Locate and identify every blood parasite.
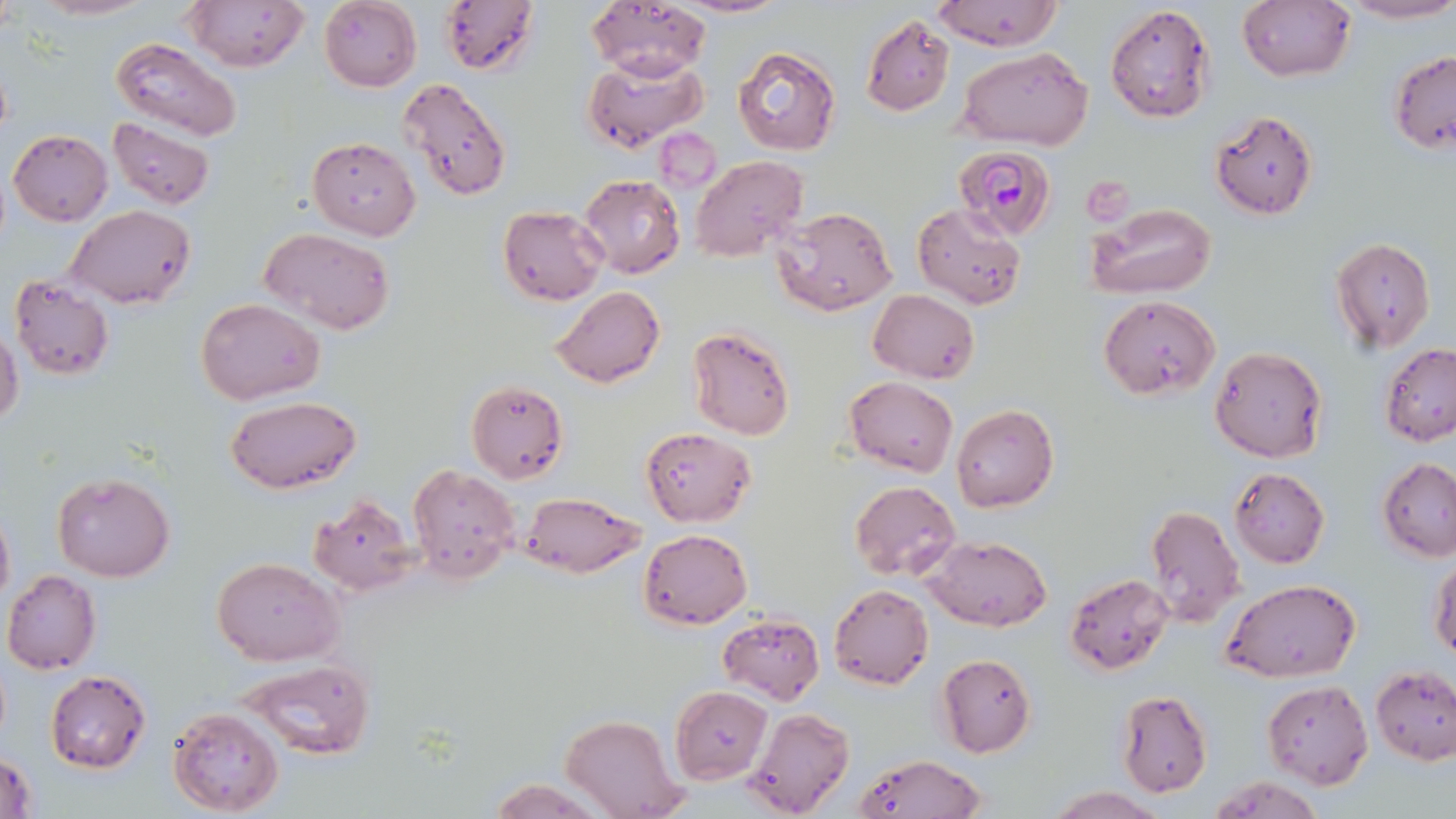

Approximate bounding boxes as (x1,y1)-(x2,y2) corner pairs in pixels.
Plasmodium falciparum-infected red blood cells: (954,145)-(1059,240).
No Plasmodium ovale, Plasmodium malariae, Plasmodium vivax, Babesia divergens, or Trypanosoma brucei observed.

Uninfected red blood cell locations: (27,0)-(157,21), (319,0)-(422,91), (439,0)-(539,76), (675,0)-(788,18), (931,0)-(1063,51), (1335,0)-(1456,24), (183,1)-(309,71), (585,1)-(711,81), (1237,2)-(1355,82), (1105,4)-(1213,123), (862,16)-(953,115), (110,37)-(244,143), (730,45)-(842,158), (958,46)-(1094,148), (1388,50)-(1456,154), (580,56)-(708,153), (397,76)-(513,202), (1211,110)-(1318,220), (108,120)-(215,210), (655,127)-(720,193), (8,129)-(111,226), (307,137)-(420,240), (691,156)-(807,262), (579,175)-(685,277), (911,203)-(1028,311), (1087,203)-(1216,299), (68,205)-(196,309), (498,206)-(607,304), (771,206)-(897,316), (257,227)-(396,335), (1331,238)-(1436,354), (9,275)-(115,381), (552,285)-(665,388), (869,290)-(979,383), (1097,295)-(1220,399), (196,297)-(325,404), (0,326)-(23,430), (686,326)-(795,440), (1381,344)-(1456,446), (1209,345)-(1328,464), (845,375)-(957,477), (465,379)-(568,483), (225,396)-(361,495), (951,405)-(1059,514), (642,427)-(756,526), (1378,457)-(1456,562), (407,465)-(520,582), (1229,467)-(1330,567), (52,471)-(176,584), (848,481)-(961,579), (521,491)-(645,579), (307,495)-(417,596), (0,499)-(13,612), (1144,504)-(1245,627), (639,528)-(752,629), (920,535)-(1052,632), (212,556)-(343,666), (1429,556)-(1456,659), (2,570)-(100,675), (1064,572)-(1175,674), (1222,577)-(1362,682), (828,582)-(933,690), (718,612)-(825,705), (936,654)-(1036,757), (240,660)-(373,764), (1371,666)-(1456,764), (44,669)-(151,773), (1262,679)-(1374,789), (669,688)-(771,783), (1115,689)-(1213,798), (167,705)-(285,816), (744,707)-(854,819), (560,715)-(686,819), (852,753)-(989,818), (0,754)-(37,819), (1204,775)-(1324,818), (485,776)-(607,817), (1042,787)-(1169,819). Slide-level diagnosis: Plasmodium falciparum. Optical microscopy. Single field of view. Thin blood smear. May-Grünwald-Giemsa stain. 1000x magnification. Image is 1456×819 pixels.